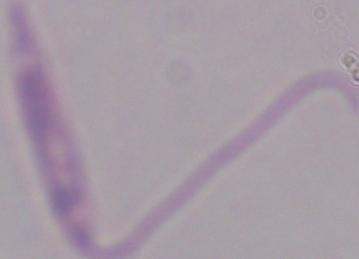
{
  "modality": "photomicrograph",
  "magnification": "1000x",
  "identification": "Leishmania"
}